Locate every blood parasite and identify its species.
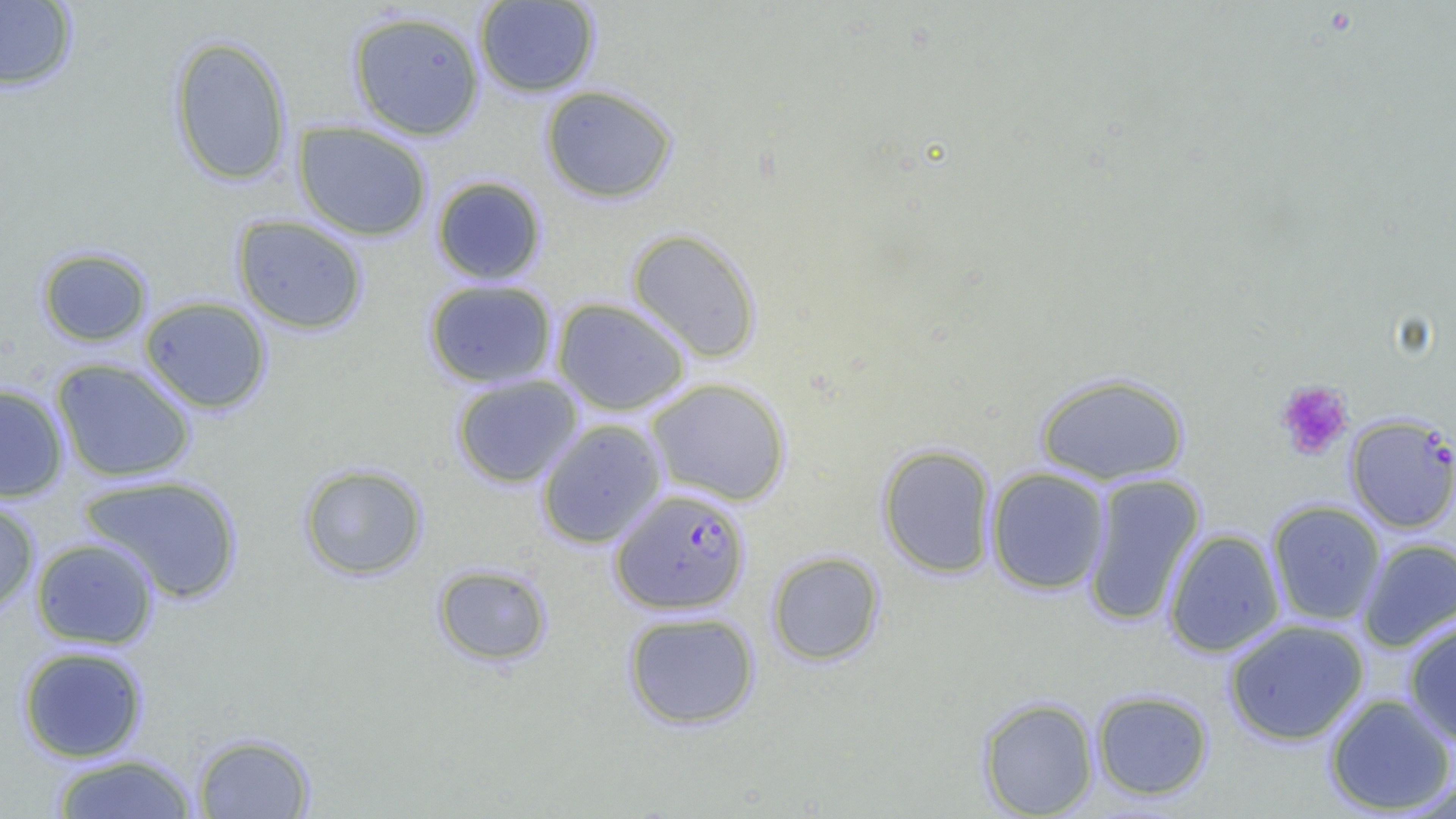
Approximate bounding boxes as (x1, y1, x2, y2) in pixels.
Plasmodium falciparum-infected red blood cells: (1346, 414, 1456, 533), (610, 487, 750, 614).
No Plasmodium ovale, Plasmodium malariae, Plasmodium vivax, Babesia divergens, or Trypanosoma brucei observed.

slide-level diagnosis = Plasmodium falciparum
uninfected red blood cell locations = approximate bounding boxes as (x1, y1, x2, y2) in pixels: (0, 1, 78, 92), (474, 1, 600, 97), (347, 9, 486, 141), (168, 35, 293, 187), (540, 84, 677, 204), (293, 121, 432, 241), (431, 176, 547, 285), (232, 215, 369, 334), (626, 228, 762, 362), (36, 246, 152, 347), (423, 279, 558, 388), (139, 296, 273, 414), (551, 297, 692, 416), (51, 359, 196, 484), (1035, 372, 1190, 485), (451, 374, 583, 488), (644, 377, 792, 506), (0, 383, 69, 503), (535, 418, 668, 549), (877, 444, 998, 578), (298, 462, 429, 581), (985, 467, 1111, 595), (1082, 473, 1205, 626), (79, 474, 244, 605), (0, 496, 41, 617), (1266, 500, 1386, 626), (1163, 528, 1286, 658), (30, 537, 159, 649), (1357, 538, 1456, 652), (766, 550, 886, 666), (431, 563, 553, 666), (622, 610, 760, 730), (1402, 617, 1456, 747), (1223, 619, 1370, 746), (17, 645, 149, 763), (1091, 689, 1214, 802), (1323, 692, 1456, 815), (978, 697, 1099, 818), (193, 732, 315, 818), (49, 752, 200, 818)
image size = 1456×819 pixels
field of view = one of a larger specimen
modality = optical microscopy
preparation = thin blood film
magnification = 1000x
platelet locations = approximate bounding boxes as (x1, y1, x2, y2) in pixels: (1275, 380, 1353, 461)